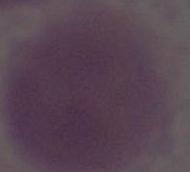
Captured at 1000x magnification. Micrograph. An erythrocyte is seen.